Name the parasite shown.
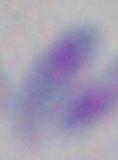
This is Toxoplasma gondii.

Summary:
  - Magnification: 1000x
  - Modality: micrograph